Give the extent of all Plasmodium falciparum-infected red blood cells.
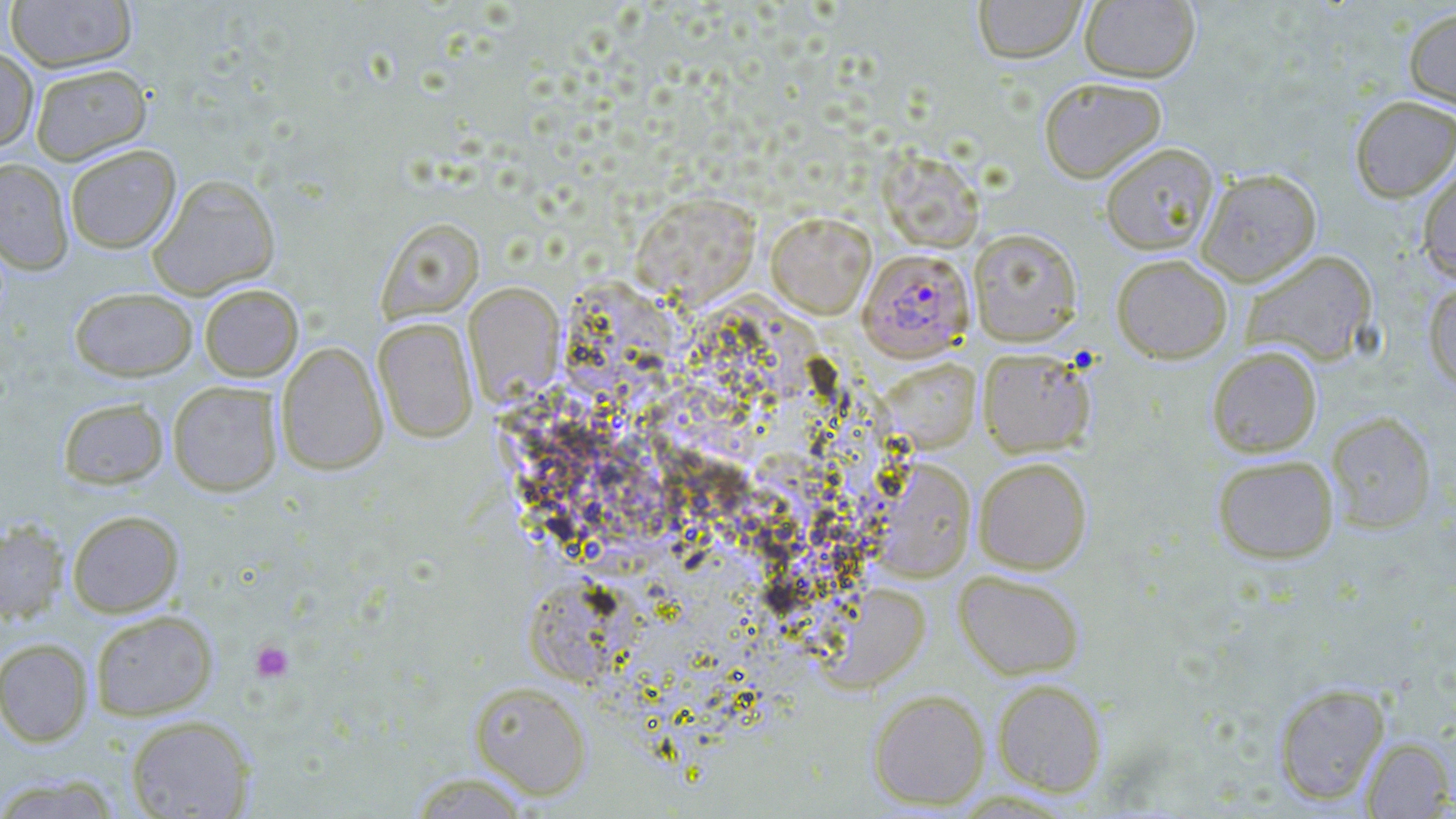

Approximate bounding boxes as (x1, y1, x2, y2) in pixels.
Plasmodium falciparum-infected red blood cells: (858, 248, 974, 361).

slide-level diagnosis = Plasmodium falciparum
preparation = thin blood film
uninfected red blood cell locations = approximate bounding boxes as (x1, y1, x2, y2) in pixels: (5, 0, 137, 73), (973, 0, 1086, 64), (1079, 1, 1200, 83), (1403, 6, 1456, 111), (0, 46, 39, 150), (29, 63, 151, 165), (1038, 76, 1167, 183), (1350, 95, 1456, 202), (1100, 142, 1220, 255), (64, 144, 181, 253), (878, 148, 985, 252), (0, 158, 73, 273), (1417, 160, 1456, 283), (1196, 168, 1321, 286), (147, 174, 281, 299), (631, 191, 761, 306), (766, 212, 875, 318), (376, 217, 484, 322), (968, 227, 1083, 345), (1240, 249, 1379, 367), (1111, 253, 1233, 364), (559, 280, 677, 408), (1423, 281, 1456, 393), (463, 282, 564, 404), (199, 284, 303, 381), (69, 286, 198, 381), (372, 317, 478, 443), (276, 341, 387, 476), (1206, 345, 1322, 457), (977, 347, 1096, 457), (880, 358, 981, 451), (167, 380, 283, 496), (57, 397, 169, 490), (1326, 411, 1437, 533), (1212, 454, 1339, 564), (973, 456, 1092, 574), (877, 460, 975, 581), (67, 510, 184, 617), (0, 520, 69, 624), (953, 569, 1085, 680), (819, 582, 929, 691), (90, 609, 218, 720), (0, 638, 93, 747), (992, 678, 1107, 796), (469, 681, 592, 799), (1273, 682, 1390, 805), (868, 689, 989, 810), (125, 714, 256, 818), (1361, 736, 1454, 818), (406, 770, 534, 818), (0, 774, 122, 818)
platelet locations = approximate bounding boxes as (x1, y1, x2, y2) in pixels: (251, 640, 294, 682)
modality = light microscopy
stain = May-Grünwald-Giemsa
field of view = one of a larger specimen
magnification = 1000x
image size = 1456×819 pixels